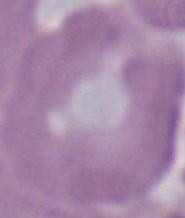
Summary:
  - Magnification: 1000x
  - Identification: erythrocyte
  - Modality: photomicrograph